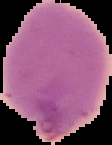
Summary:
  - Preparation: thin blood smear
  - Image type: segmented cell region with the area outside set to black
  - Malaria status: uninfected
  - Image size: 112×145 pixels